Report the malaria status of this cell.
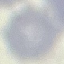

Uninfected.

Cell patch, automatically extracted from a larger field of view and resized to 64 × 64 pixels. Photographed with a smartphone camera at the microscope eyepiece. Giemsa stain. Thin blood smear.